Name the cell type shown.
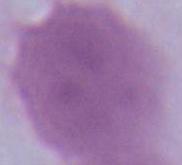
This is an erythrocyte.

Summary:
  - Modality: photomicrograph
  - Magnification: 1000x